Locate every uninfected red blood cell.
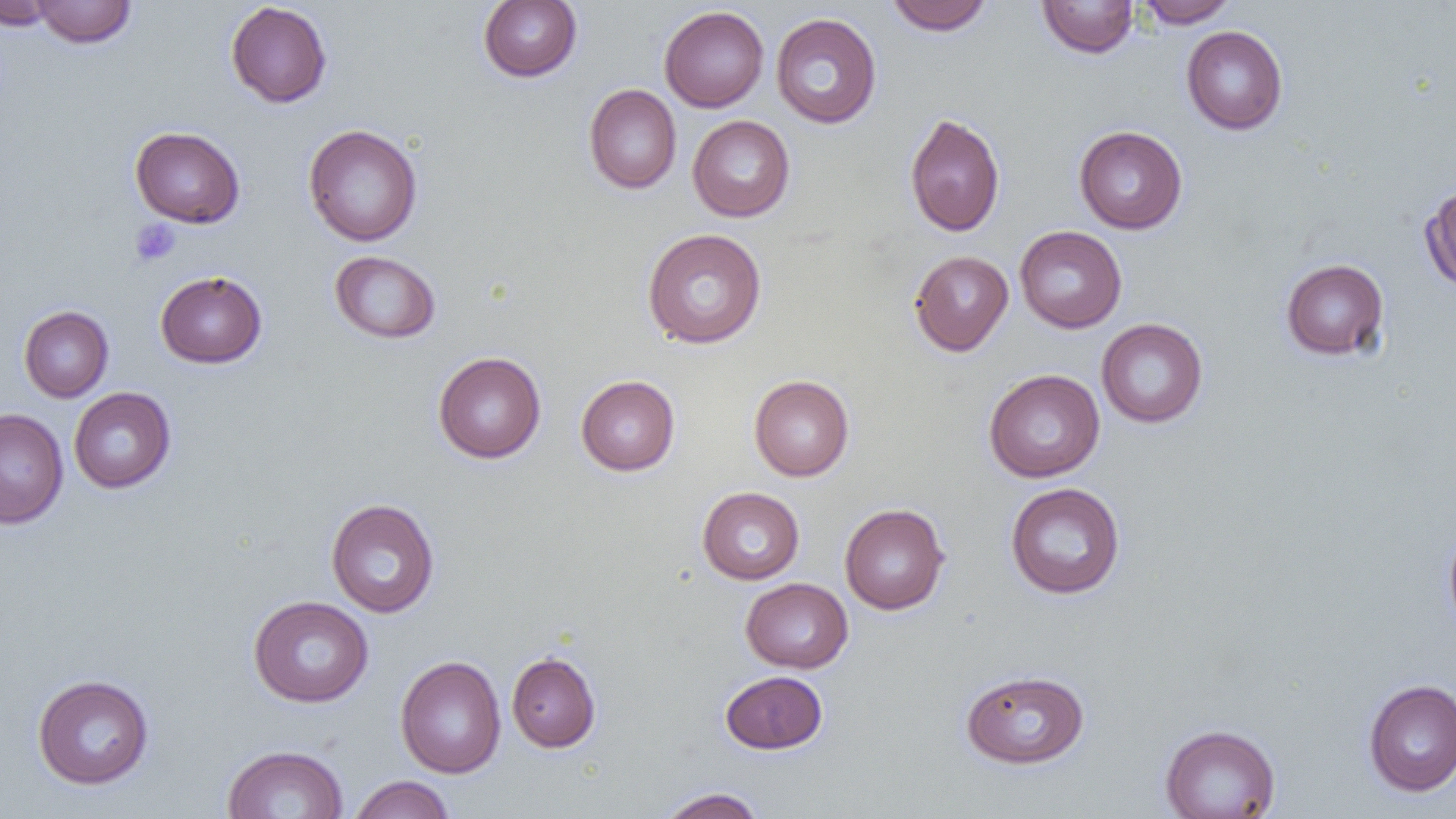

Approximate bounding boxes as named x1/y1/x2/y2 corners in pixels.
Uninfected red blood cells: (x1=0, y1=0, x2=59, y2=30), (x1=32, y1=0, x2=136, y2=48), (x1=885, y1=0, x2=994, y2=36), (x1=1136, y1=0, x2=1238, y2=27), (x1=478, y1=1, x2=582, y2=82), (x1=1037, y1=1, x2=1139, y2=58), (x1=225, y1=2, x2=332, y2=108), (x1=659, y1=5, x2=769, y2=112), (x1=770, y1=12, x2=882, y2=129), (x1=1181, y1=25, x2=1288, y2=134), (x1=583, y1=84, x2=682, y2=194), (x1=904, y1=113, x2=1005, y2=236), (x1=687, y1=115, x2=795, y2=221), (x1=303, y1=124, x2=422, y2=247), (x1=1074, y1=125, x2=1188, y2=234), (x1=130, y1=126, x2=245, y2=228), (x1=1420, y1=182, x2=1456, y2=293), (x1=1015, y1=225, x2=1127, y2=332), (x1=641, y1=228, x2=767, y2=349), (x1=329, y1=250, x2=441, y2=344), (x1=909, y1=250, x2=1013, y2=356), (x1=1281, y1=258, x2=1390, y2=360), (x1=155, y1=270, x2=267, y2=368), (x1=18, y1=305, x2=114, y2=402), (x1=1096, y1=318, x2=1208, y2=428), (x1=433, y1=351, x2=546, y2=463), (x1=984, y1=369, x2=1105, y2=482), (x1=749, y1=374, x2=854, y2=480), (x1=575, y1=375, x2=680, y2=475), (x1=69, y1=387, x2=176, y2=493), (x1=0, y1=407, x2=68, y2=529), (x1=1005, y1=482, x2=1126, y2=599), (x1=696, y1=486, x2=804, y2=584), (x1=325, y1=498, x2=439, y2=618), (x1=839, y1=503, x2=950, y2=615), (x1=1443, y1=526, x2=1456, y2=635), (x1=740, y1=577, x2=853, y2=673), (x1=248, y1=595, x2=374, y2=707), (x1=506, y1=651, x2=601, y2=752), (x1=395, y1=655, x2=506, y2=778), (x1=960, y1=669, x2=1090, y2=769), (x1=719, y1=670, x2=828, y2=754), (x1=32, y1=674, x2=155, y2=790), (x1=1363, y1=679, x2=1456, y2=796), (x1=1160, y1=723, x2=1281, y2=818), (x1=221, y1=745, x2=349, y2=819), (x1=348, y1=775, x2=455, y2=819), (x1=657, y1=787, x2=767, y2=818).

{
  "slide_level_diagnosis": "negative for blood parasites",
  "platelet_locations": "approximate bounding boxes as named x1/y1/x2/y2 corners in pixels: (x1=130, y1=219, x2=181, y2=267)",
  "image_size": "1456×819 pixels",
  "field_of_view": "one of a larger specimen",
  "magnification": "1000x",
  "modality": "light microscopy",
  "preparation": "thin blood film"
}